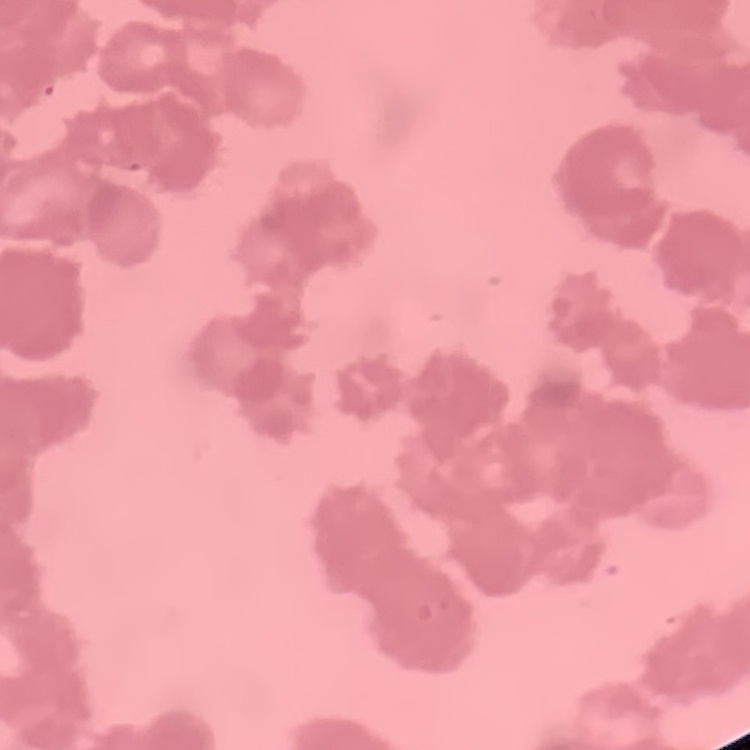 The erythrocytes exhibit rouleaux formation. Field's or Giemsa stain. One tile cut from a larger photomicrograph. Thin blood smear.